Give the position of every Plasmodium parasite.
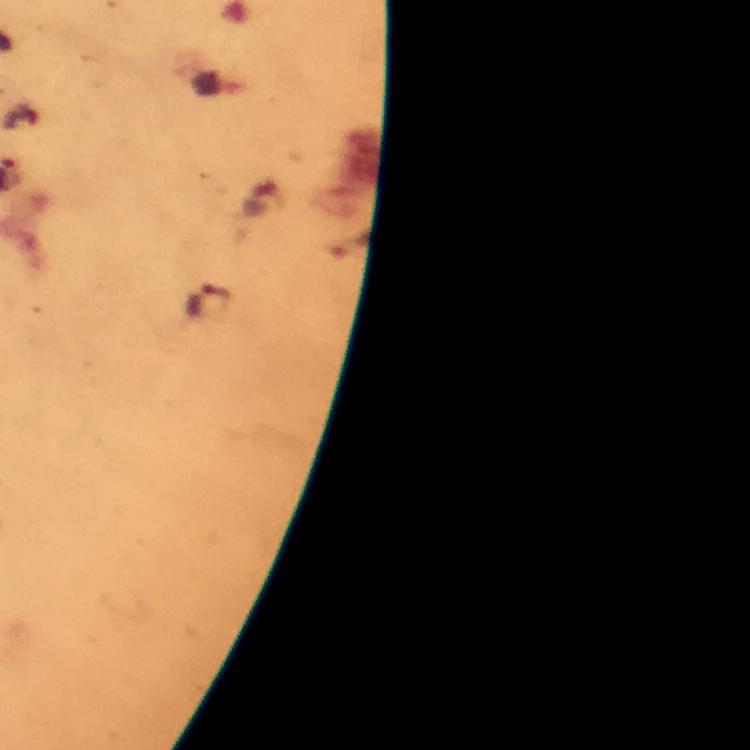

Approximate centers as [x, y] in pixels.
Plasmodium parasites: [209, 301].

context = from a malaria diagnostic workup
immersion oil = applied
magnification = 100x
stain = Giemsa
image size = 750×750 pixels
preparation = thick smear
capture = smartphone camera through the microscope
cropped from = one field of view